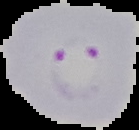
{
  "image_size": "139×130 pixels",
  "preparation": "thin blood smear",
  "malaria_status": "parasitized",
  "image_type": "segmented cell region on a black background"
}